Comment on the morphology of the erythrocytes.
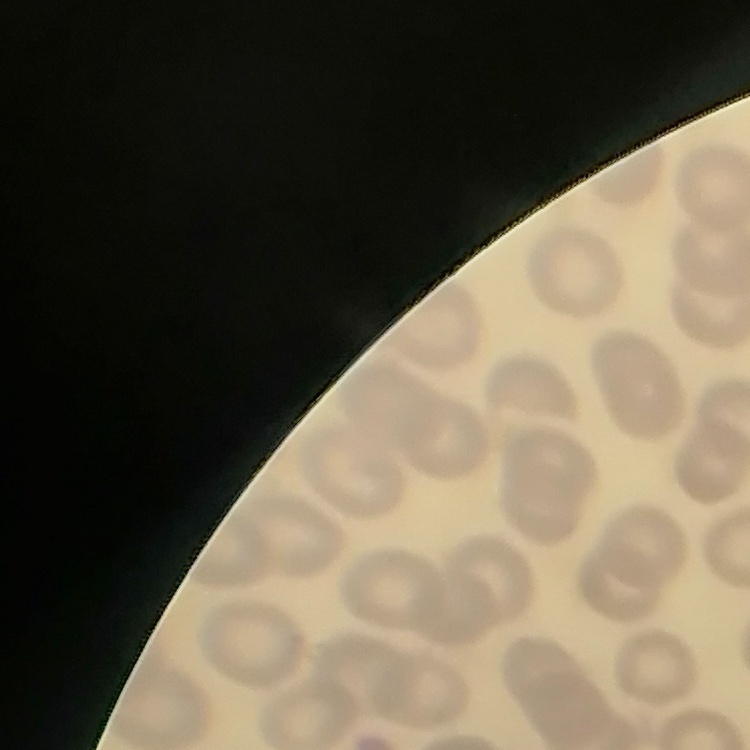

They show no rouleaux formation.

Summary:
  - Stain: Field's or Giemsa
  - Image type: square crop of a larger photomicrograph
  - Preparation: thin peripheral smear